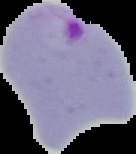

{
  "malaria_status": "parasitized",
  "image_type": "segmented cell region with the area outside set to black",
  "preparation": "thin blood smear",
  "image_size": "136×154 pixels"
}